Report the malaria status of this cell.
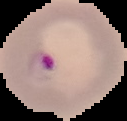
It is parasitized.

Summary:
  - Image type: segmented cell region with the area outside set to black
  - Preparation: thin blood smear
  - Image size: 127×121 pixels